Locate and identify every blood parasite.
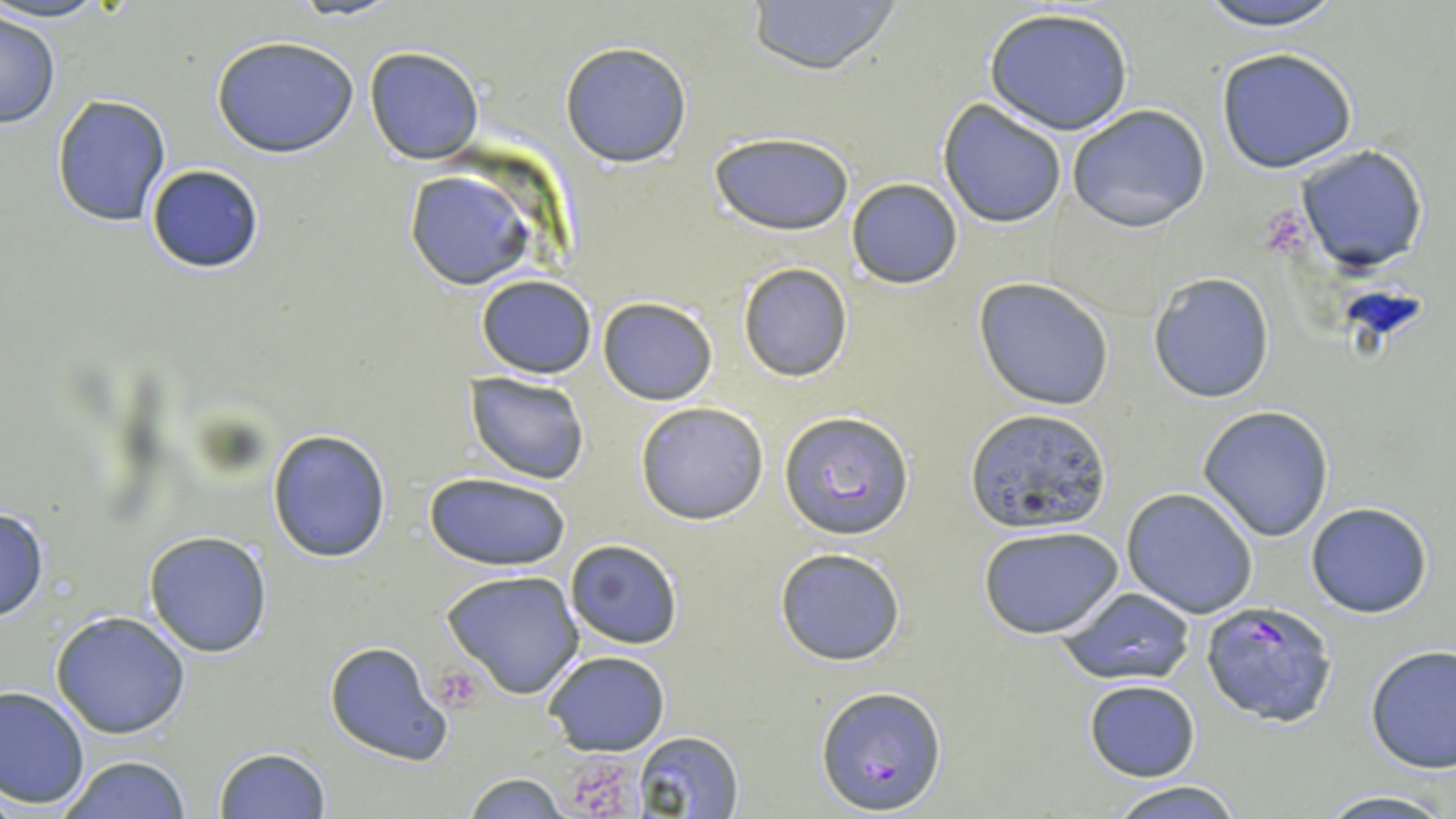

Approximate bounding boxes as named x1/y1/x2/y2 corners in pixels.
Plasmodium falciparum-infected red blood cells (subset): (x1=1199, y1=600, x2=1339, y2=728), (x1=816, y1=684, x2=945, y2=814).
No Plasmodium ovale, Plasmodium malariae, Plasmodium vivax, Babesia divergens, or Trypanosoma brucei observed.

Summary:
  - Platelet locations: (x1=437, y1=666, x2=485, y2=708), (x1=567, y1=750, x2=645, y2=819)
  - Uninfected red blood cell locations (subset): (x1=742, y1=0, x2=903, y2=74), (x1=1190, y1=0, x2=1350, y2=29), (x1=982, y1=4, x2=1136, y2=136), (x1=0, y1=14, x2=60, y2=128), (x1=211, y1=35, x2=359, y2=158), (x1=559, y1=41, x2=692, y2=168), (x1=364, y1=46, x2=485, y2=165), (x1=1216, y1=48, x2=1358, y2=174), (x1=51, y1=93, x2=172, y2=228), (x1=938, y1=99, x2=1068, y2=228), (x1=1067, y1=103, x2=1211, y2=232), (x1=710, y1=132, x2=856, y2=236), (x1=1294, y1=144, x2=1430, y2=274), (x1=145, y1=164, x2=266, y2=274), (x1=404, y1=169, x2=534, y2=291), (x1=846, y1=178, x2=964, y2=289), (x1=737, y1=263, x2=853, y2=382), (x1=1147, y1=272, x2=1276, y2=403), (x1=475, y1=274, x2=597, y2=377), (x1=974, y1=278, x2=1114, y2=411), (x1=598, y1=297, x2=718, y2=405), (x1=466, y1=372, x2=591, y2=485), (x1=635, y1=402, x2=769, y2=523), (x1=963, y1=405, x2=1110, y2=534), (x1=1197, y1=405, x2=1335, y2=542), (x1=267, y1=427, x2=392, y2=562), (x1=423, y1=474, x2=573, y2=571), (x1=1121, y1=487, x2=1260, y2=619), (x1=1305, y1=501, x2=1433, y2=619), (x1=0, y1=504, x2=49, y2=623), (x1=977, y1=524, x2=1124, y2=640), (x1=143, y1=530, x2=273, y2=658), (x1=565, y1=538, x2=683, y2=650), (x1=773, y1=546, x2=906, y2=666), (x1=440, y1=568, x2=586, y2=700), (x1=1058, y1=587, x2=1195, y2=688), (x1=51, y1=610, x2=191, y2=740), (x1=325, y1=640, x2=453, y2=766), (x1=1364, y1=646, x2=1456, y2=773), (x1=543, y1=650, x2=671, y2=756), (x1=1082, y1=680, x2=1200, y2=782), (x1=0, y1=684, x2=90, y2=809), (x1=631, y1=731, x2=745, y2=818), (x1=212, y1=747, x2=331, y2=819), (x1=57, y1=754, x2=195, y2=819), (x1=459, y1=772, x2=582, y2=818), (x1=1106, y1=779, x2=1246, y2=818), (x1=1312, y1=791, x2=1455, y2=819)
  - Slide-level diagnosis: Plasmodium falciparum
  - Image size: 1456×819 pixels
  - Stain: May-Grünwald-Giemsa
  - Preparation: thin blood smear
  - Modality: optical microscopy
  - Field of view: single
  - Magnification: 1000x